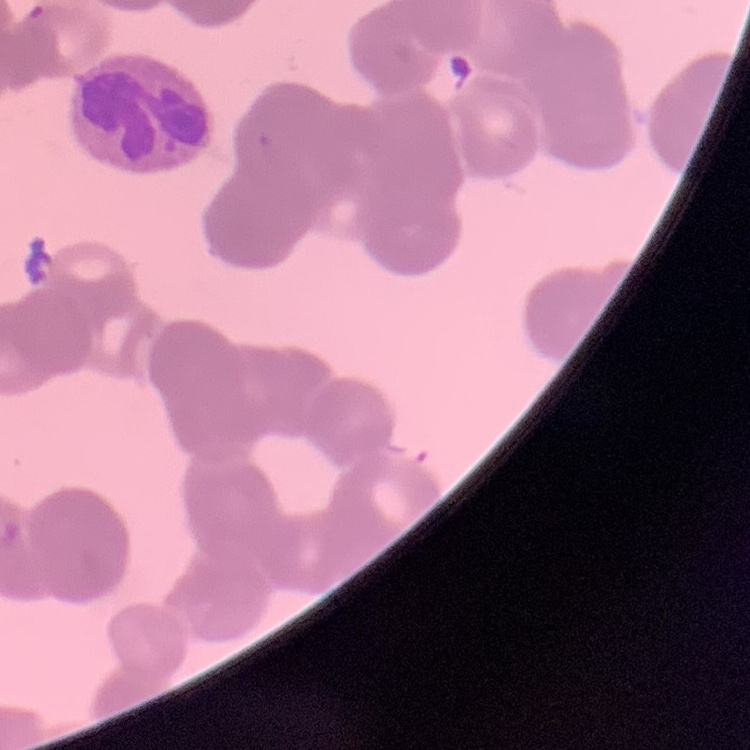

Summary:
  - Red blood cell morphology: rouleaux formation
  - Image type: one tile cut from a larger photomicrograph
  - Preparation: thin blood film
  - Stain: Field's or Giemsa